Give the extent of all Plasmodium malariae-infected red blood cells.
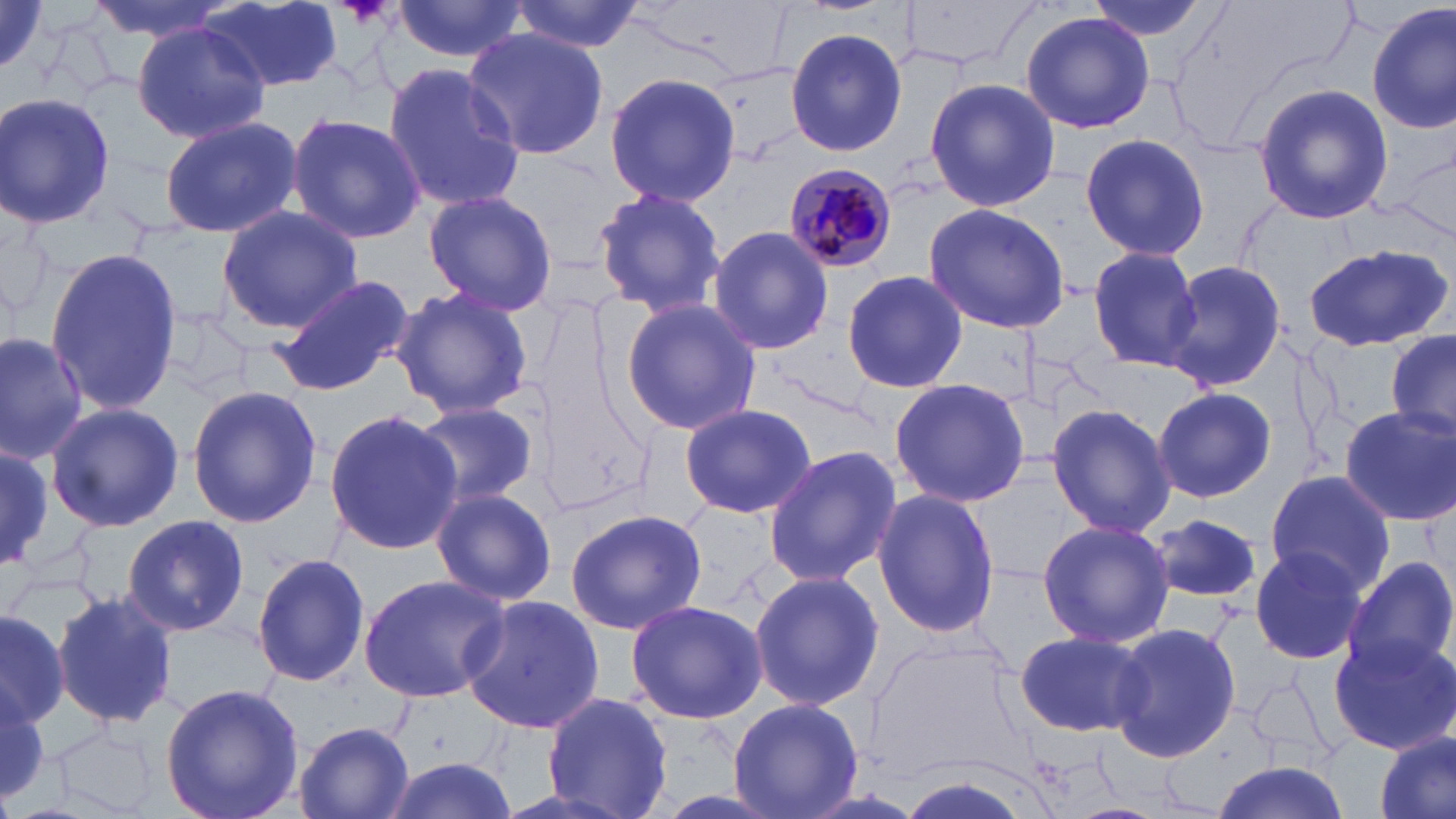
Approximate bounding boxes as [x1, y1, x2, y2] in pixels.
Plasmodium malariae-infected red blood cells: [781, 163, 898, 272].

slide-level diagnosis = Plasmodium malariae
preparation = thin blood film
stain = May-Grünwald-Giemsa
modality = light microscopy
image size = 1456×819 pixels
uninfected red blood cell locations = approximate bounding boxes as [x1, y1, x2, y2] in pixels: [0, 0, 56, 80], [84, 0, 239, 43], [391, 0, 528, 63], [510, 0, 645, 54], [1079, 0, 1219, 41], [202, 2, 344, 92], [1368, 3, 1455, 136], [1018, 10, 1157, 134], [133, 21, 270, 144], [784, 26, 908, 157], [463, 27, 609, 161], [383, 61, 525, 213], [604, 71, 739, 209], [924, 78, 1061, 211], [1253, 84, 1392, 224], [0, 92, 118, 232], [287, 113, 425, 245], [157, 115, 301, 239], [1076, 132, 1210, 262], [589, 184, 732, 321], [423, 189, 559, 317], [920, 203, 1072, 335], [215, 205, 362, 334], [708, 226, 835, 356], [1304, 240, 1453, 354], [1086, 247, 1202, 371], [44, 248, 184, 415], [1163, 259, 1287, 395], [841, 268, 966, 394], [265, 275, 415, 397], [389, 285, 535, 421], [617, 298, 763, 435], [155, 307, 260, 397], [0, 330, 88, 464], [1383, 330, 1456, 444], [887, 377, 1031, 506], [186, 384, 321, 527], [1153, 387, 1275, 502], [408, 401, 541, 509], [678, 402, 816, 521], [1046, 402, 1176, 539], [45, 403, 184, 532], [1337, 406, 1455, 527], [323, 407, 464, 557], [0, 445, 55, 573], [762, 446, 900, 586], [1264, 471, 1393, 594], [431, 486, 558, 605], [871, 487, 1004, 639], [564, 508, 706, 636], [1146, 511, 1267, 607], [121, 514, 251, 638], [1035, 517, 1174, 649], [1248, 545, 1368, 667], [252, 552, 371, 688], [1346, 554, 1456, 675], [747, 568, 886, 711], [360, 572, 509, 704], [51, 591, 179, 727], [460, 594, 603, 736], [624, 600, 769, 723], [0, 605, 70, 729], [1108, 623, 1244, 767], [1013, 628, 1152, 739], [1326, 630, 1456, 755], [158, 681, 304, 819], [0, 682, 52, 805], [543, 692, 675, 818], [726, 695, 867, 818], [294, 719, 417, 819], [1374, 729, 1455, 819], [376, 758, 518, 818], [1208, 760, 1353, 819]
field of view = single
magnification = 1000x